State the preparation type.
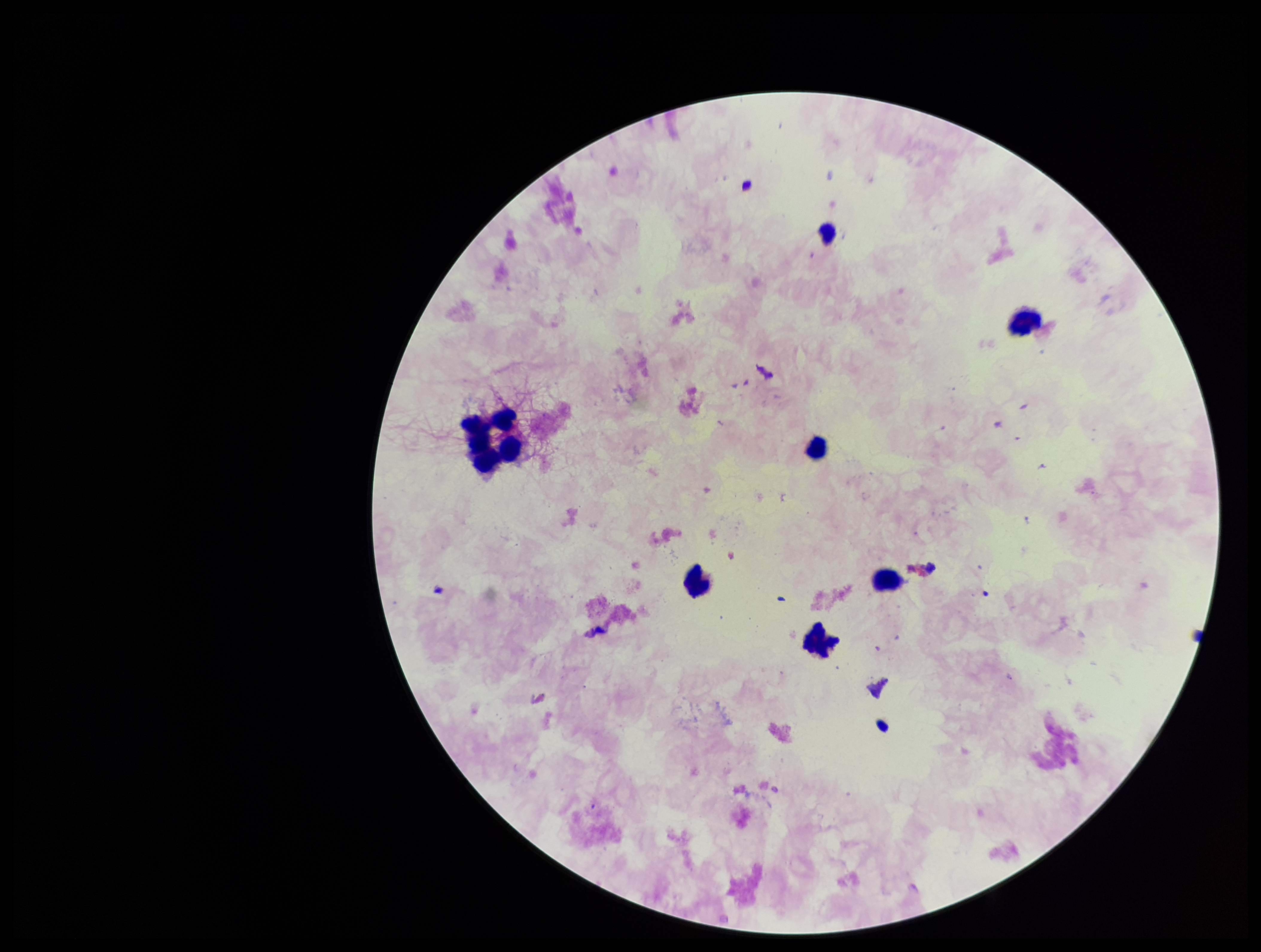

It is a thick blood smear.

Summary:
  - Image size: 1261×952 pixels
  - Field of view: single
  - Stain: Giemsa
  - Parasite count: 0
  - Patient malaria status: negative
  - Plasmodium parasites: none seen
  - Leukocyte count: 7
  - Capture: smartphone photograph through the microscope eyepiece